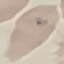

Summary:
  - Malaria status: uninfected
  - Stain: Giemsa
  - Preparation: thin smear
  - Image type: automatically extracted cell patch, resized to 64 × 64 pixels
  - Capture: smartphone through the microscope eyepiece